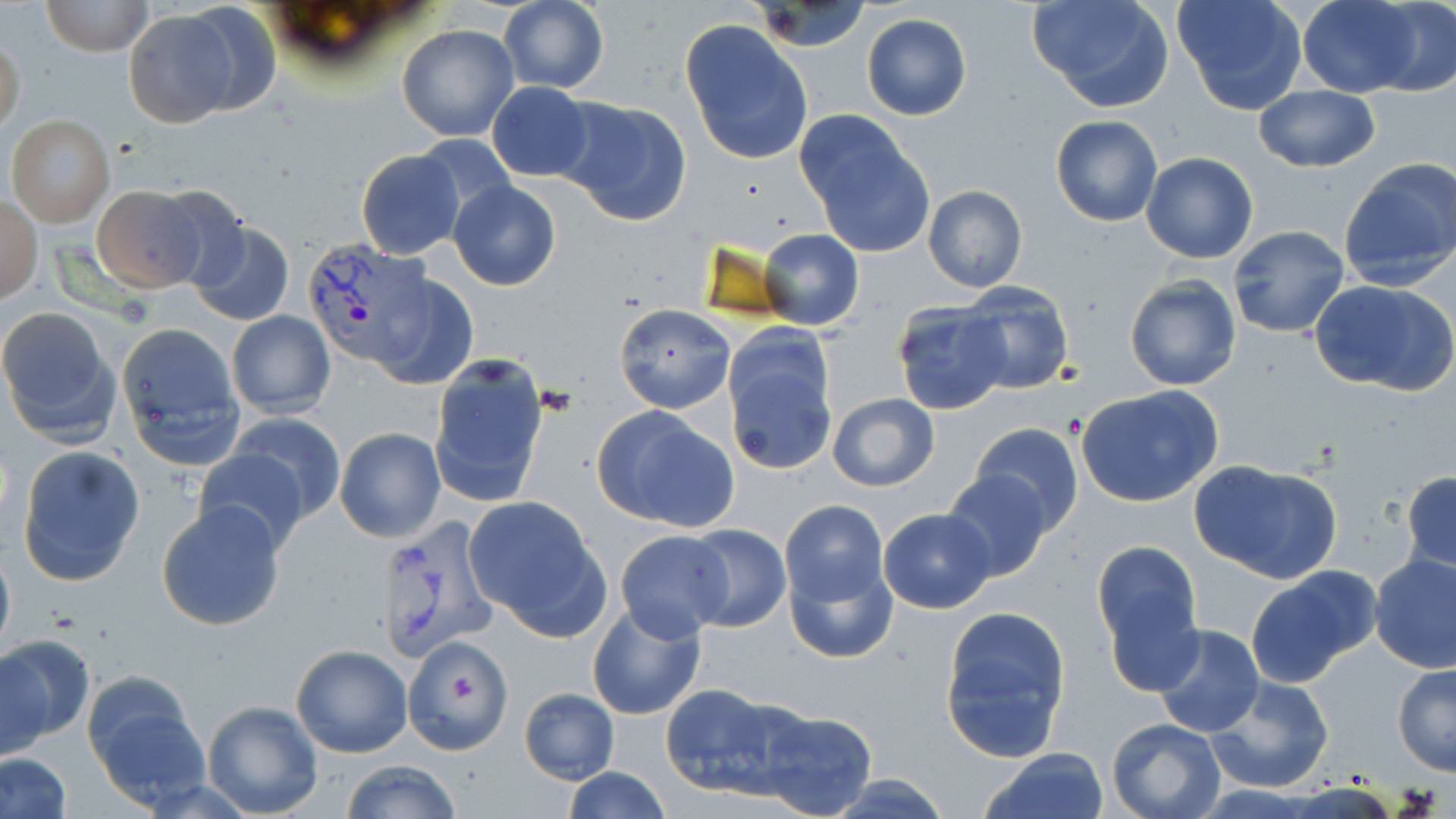 Approximate bounding boxes as [x1, y1, x2, y2] in pixels. Platelet locations: [449, 675, 477, 703]. Plasmodium vivax-infected red blood cell locations: [303, 237, 430, 368], [374, 512, 497, 665]. Uninfected red blood cell locations: [41, 0, 151, 55], [1029, 0, 1175, 113], [1173, 0, 1308, 116], [1297, 0, 1424, 97], [497, 1, 610, 94], [1367, 1, 1455, 94], [750, 2, 872, 53], [180, 3, 282, 117], [123, 9, 238, 129], [862, 14, 971, 121], [681, 21, 813, 165], [396, 24, 519, 141], [1, 33, 25, 135], [486, 81, 595, 182], [1252, 84, 1381, 173], [554, 95, 693, 228], [796, 111, 935, 260], [6, 115, 114, 226], [1050, 115, 1162, 226], [415, 134, 517, 225], [355, 148, 465, 260], [1140, 151, 1258, 264], [1339, 158, 1456, 291], [448, 180, 563, 291], [92, 185, 206, 293], [148, 185, 249, 289], [922, 185, 1028, 293], [1, 197, 42, 303], [187, 221, 293, 328], [1228, 225, 1350, 340], [759, 229, 865, 330], [370, 272, 480, 389], [1124, 276, 1242, 391], [1308, 278, 1456, 397], [960, 284, 1076, 395], [891, 302, 1012, 415], [614, 304, 735, 415], [0, 306, 120, 445], [226, 310, 336, 418], [115, 323, 245, 469], [724, 339, 838, 475], [427, 355, 552, 508], [1075, 384, 1224, 507], [826, 392, 940, 491], [592, 406, 740, 532], [225, 413, 347, 522], [970, 422, 1084, 534], [334, 426, 446, 542], [15, 444, 145, 586], [192, 448, 308, 553], [1190, 460, 1342, 584], [939, 469, 1056, 582], [1401, 472, 1456, 571], [464, 496, 608, 637], [155, 500, 288, 633], [779, 500, 889, 609], [878, 507, 998, 614], [683, 524, 791, 633], [614, 529, 733, 641], [0, 539, 15, 665], [1095, 545, 1204, 692], [784, 552, 896, 665], [1369, 553, 1456, 673], [1245, 566, 1381, 685], [587, 601, 706, 720], [940, 607, 1073, 762], [1155, 624, 1264, 736], [0, 634, 94, 750], [404, 635, 511, 751], [1175, 639, 1312, 768], [290, 644, 414, 758], [1391, 664, 1456, 777], [82, 672, 209, 808], [1203, 674, 1333, 794], [660, 684, 797, 799], [518, 688, 620, 784], [201, 701, 324, 818], [753, 705, 878, 818], [1106, 717, 1228, 819], [980, 747, 1111, 819], [2, 753, 71, 818], [340, 760, 462, 818], [564, 766, 670, 819], [825, 774, 955, 817]. Slide-level diagnosis: Plasmodium vivax. Thin blood smear. 1000x magnification. Optical microscopy. Image is 1456×819 pixels. May-Grünwald-Giemsa-stained preparation. One field of a larger specimen.